Describe the morphology of the red blood cells.
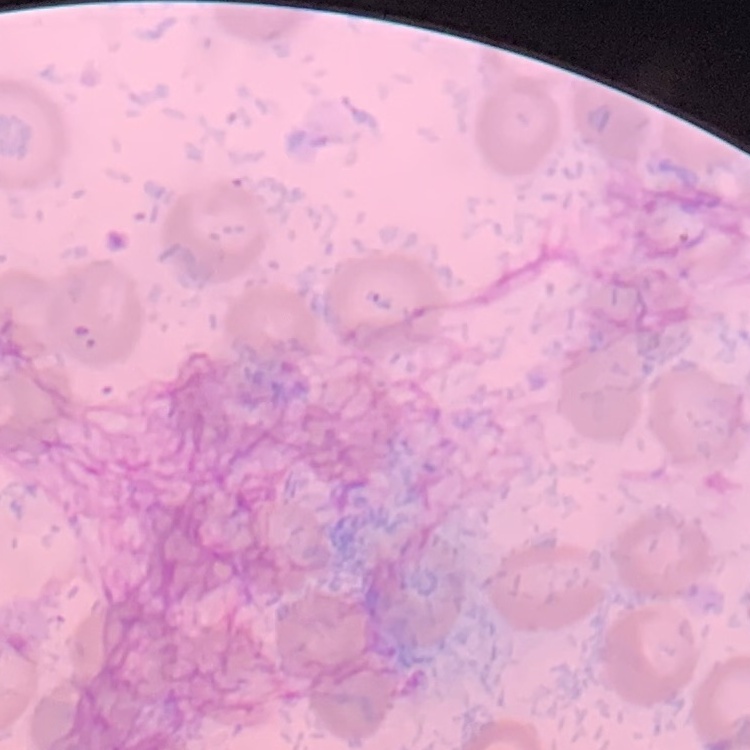

They show no rouleaux formation.

Thin blood smear. Square crop of a larger photomicrograph. Field's or Giemsa stain.